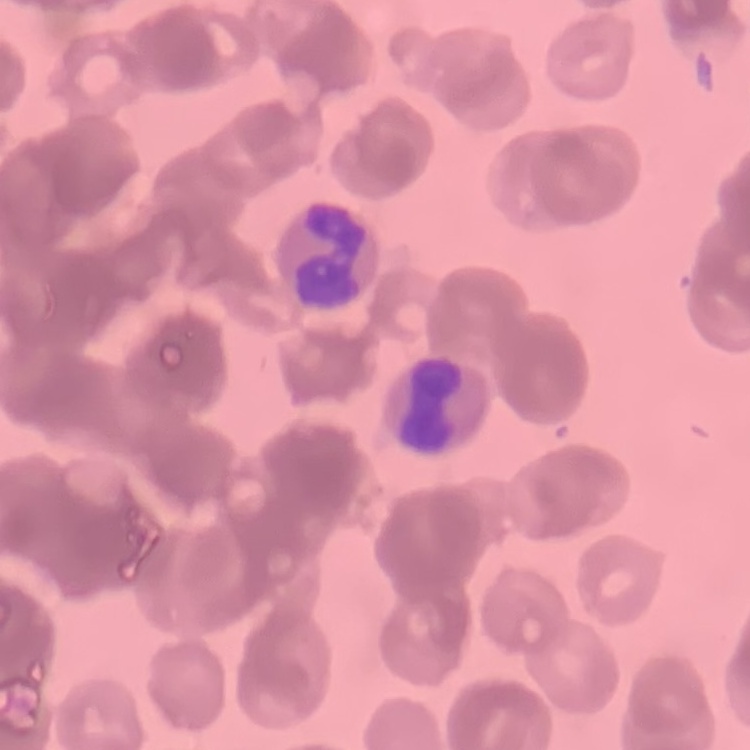

{
  "red_blood_cell_morphology": "rouleaux formation",
  "stain": "Field's or Giemsa",
  "image_type": "square crop of a larger photomicrograph",
  "preparation": "thin peripheral smear"
}